Name the parasite shown.
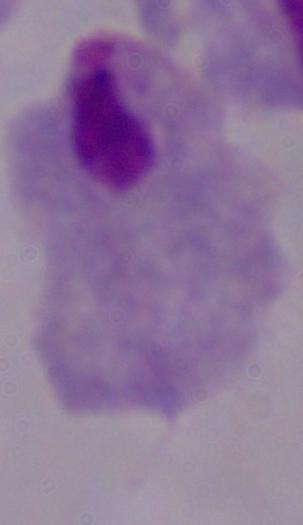
This is a trichomonad.

Micrograph. Captured at 1000x magnification.